Classify this cell by malaria status.
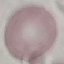
It is uninfected.

Summary:
  - Image type: cell patch, automatically extracted from a larger field of view and resized to 64 × 64 pixels
  - Stain: Giemsa
  - Preparation: thin smear
  - Capture: smartphone camera at the microscope eyepiece